Describe the morphology of the red blood cells.
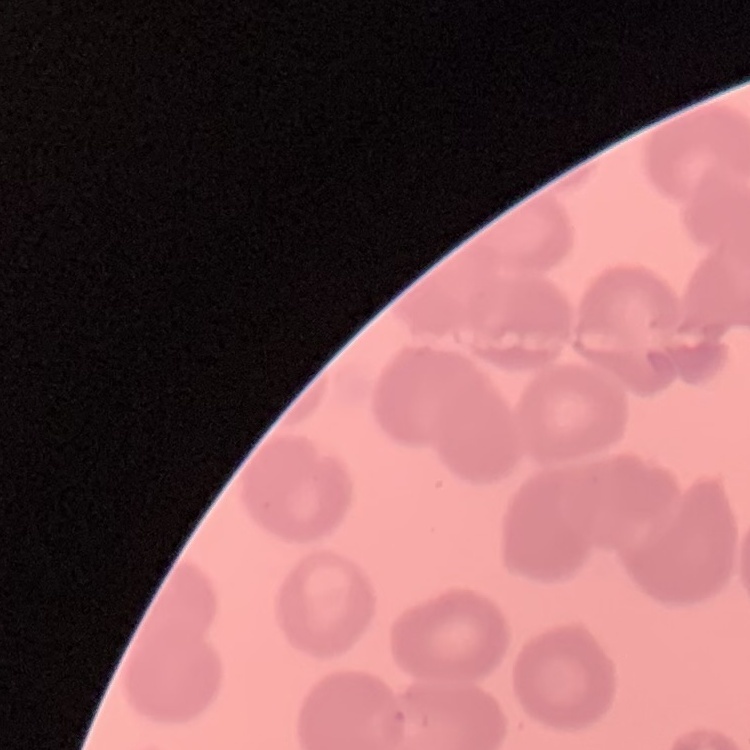

They show no rouleaux formation.

Summary:
  - Preparation: thin blood smear
  - Image type: one tile cut from a larger photomicrograph
  - Stain: Field's or Giemsa